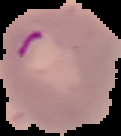
Image is 121×136 pixels. The area outside the segmented cell region is set to black. From a thin blood film. Malaria status: parasitized.